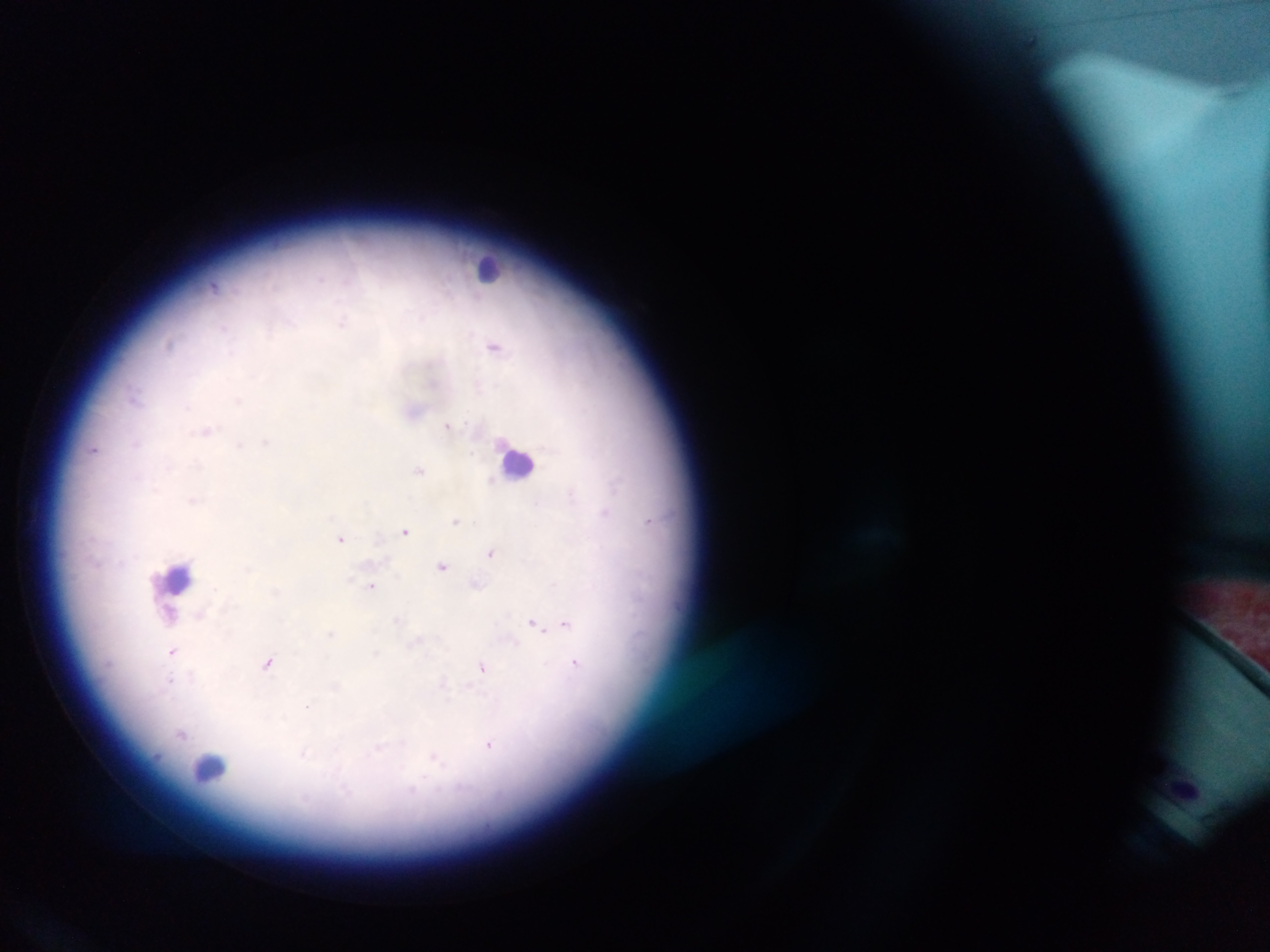

Approximate centers as x y in pixels.
Summary:
  - Leukocyte locations: 488 267; 517 462; 178 577; 210 769
  - Malaria parasite locations: 320 278; 214 286; 343 322; 223 327; 169 343; 494 346; 134 397; 239 400; 187 406; 447 424; 206 431; 266 441; 135 444; 239 445; 94 449; 420 470; 491 481; 570 493; 192 501; 604 513; 649 520; 456 521; 405 531; 340 538; 491 553; 442 567; 372 586; 477 586; 169 614; 201 616; 397 621; 533 623; 565 624; 332 633; 417 643; 172 652; 376 653; 267 663; 575 665; 482 669; 191 678; 169 681; 443 685; 308 707; 181 734; 490 744; 378 750; 303 755; 436 760; 413 790
  - Country: Ghana
  - Capture: mobile-phone photograph through a microscope
  - Preparation: thick blood smear
  - Field of view: single
  - Image size: 1270×952 pixels